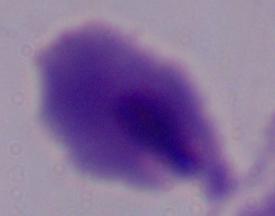

Summary:
  - Magnification: 1000x
  - Modality: micrograph
  - Identification: trichomonad